Identify the parasite.
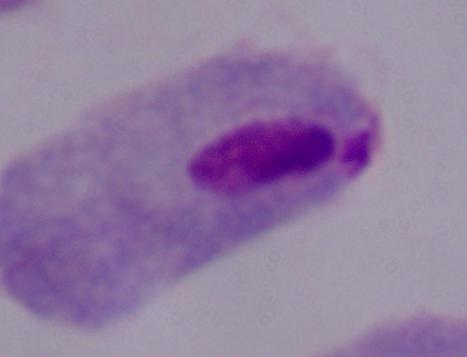

This is a trichomonad.

Summary:
  - Magnification: 1000x
  - Modality: photomicrograph